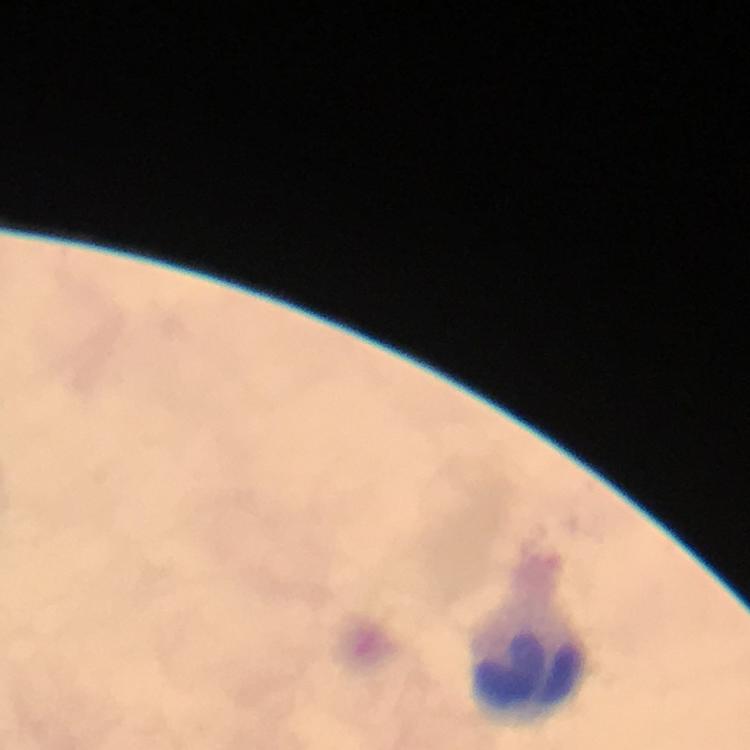
Approximate object centers, in pixels from the top-left corner.
Summary:
  - Leukocyte locations: (x=526, y=665)
  - Preparation: thick blood smear
  - Image size: 750×750 pixels
  - Capture: smartphone photograph through a microscope
  - Immersion oil: used
  - Stain: Giemsa
  - Cropped from: one field of view
  - Malaria parasites: none detected
  - Context: from a diagnostic examination for malaria
  - Magnification: 100x